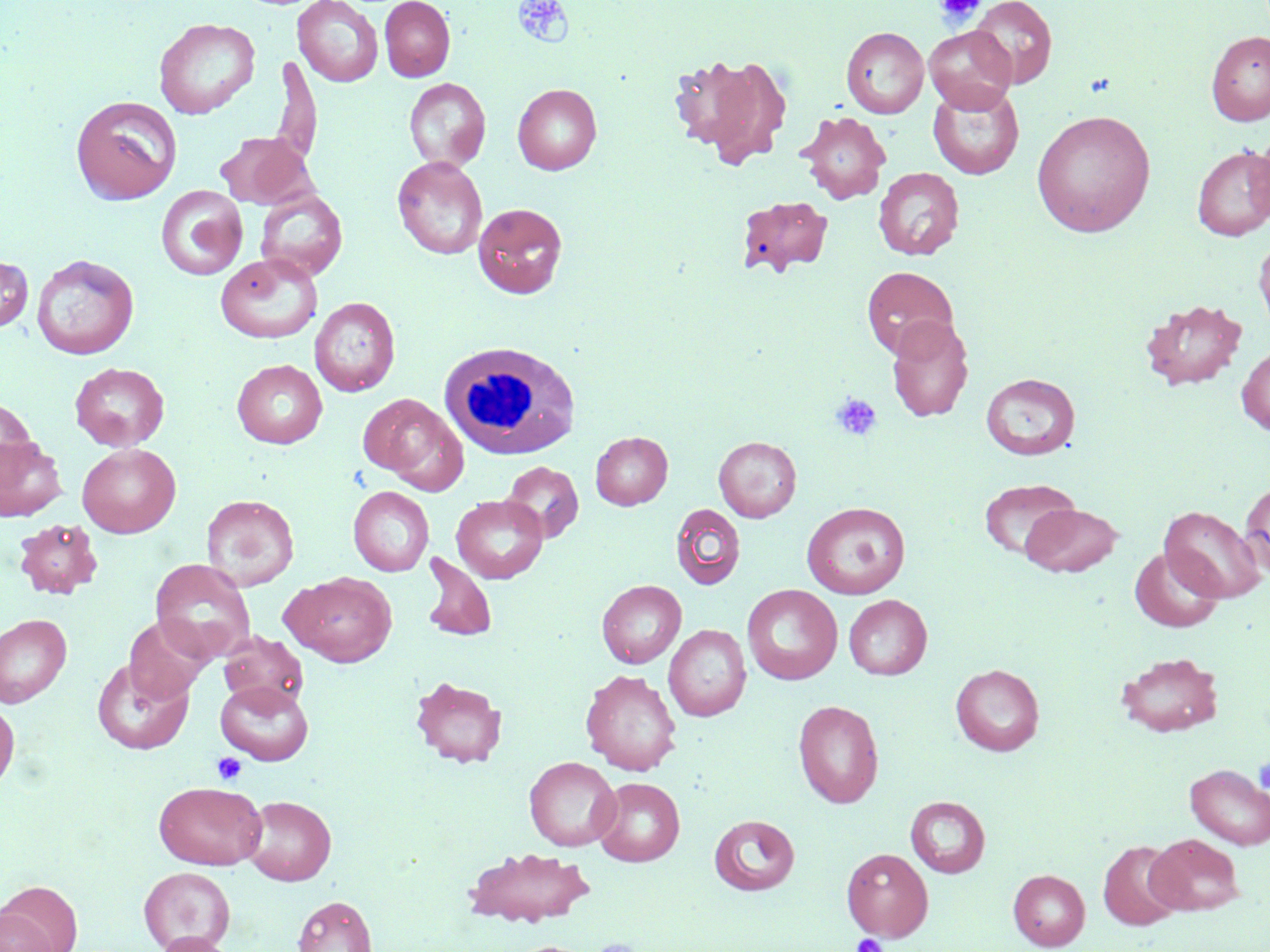

Approximate bounding boxes as named x1/y1/x2/y2 corners in pixels. Uninfected red blood cell locations: (x1=293, y1=0, x2=384, y2=87), (x1=380, y1=0, x2=455, y2=82), (x1=969, y1=0, x2=1057, y2=88), (x1=154, y1=17, x2=260, y2=119), (x1=924, y1=26, x2=1017, y2=113), (x1=841, y1=27, x2=929, y2=119), (x1=1206, y1=31, x2=1270, y2=125), (x1=668, y1=51, x2=793, y2=168), (x1=270, y1=55, x2=322, y2=169), (x1=404, y1=78, x2=491, y2=171), (x1=928, y1=83, x2=1024, y2=180), (x1=513, y1=84, x2=601, y2=175), (x1=71, y1=95, x2=181, y2=204), (x1=1031, y1=109, x2=1156, y2=237), (x1=797, y1=111, x2=891, y2=204), (x1=215, y1=131, x2=314, y2=209), (x1=1249, y1=131, x2=1270, y2=228), (x1=1192, y1=145, x2=1270, y2=241), (x1=392, y1=156, x2=488, y2=259), (x1=874, y1=167, x2=964, y2=260), (x1=156, y1=185, x2=248, y2=281), (x1=256, y1=189, x2=348, y2=282), (x1=738, y1=195, x2=833, y2=277), (x1=473, y1=202, x2=568, y2=299), (x1=1254, y1=235, x2=1270, y2=335), (x1=216, y1=253, x2=322, y2=343), (x1=0, y1=254, x2=33, y2=332), (x1=31, y1=254, x2=139, y2=359), (x1=862, y1=266, x2=958, y2=358), (x1=310, y1=296, x2=400, y2=397), (x1=1141, y1=299, x2=1247, y2=390), (x1=886, y1=316, x2=974, y2=421), (x1=1237, y1=346, x2=1270, y2=435), (x1=232, y1=359, x2=327, y2=448), (x1=70, y1=362, x2=169, y2=451), (x1=981, y1=372, x2=1081, y2=460), (x1=359, y1=393, x2=466, y2=490), (x1=0, y1=399, x2=37, y2=485), (x1=591, y1=431, x2=672, y2=510), (x1=714, y1=436, x2=801, y2=522), (x1=0, y1=437, x2=67, y2=521), (x1=77, y1=443, x2=181, y2=537), (x1=502, y1=461, x2=584, y2=543), (x1=978, y1=478, x2=1080, y2=561), (x1=1240, y1=480, x2=1270, y2=580), (x1=348, y1=486, x2=433, y2=576), (x1=201, y1=494, x2=299, y2=591), (x1=452, y1=495, x2=548, y2=583), (x1=802, y1=502, x2=910, y2=599), (x1=1020, y1=503, x2=1124, y2=576), (x1=671, y1=504, x2=745, y2=590), (x1=1159, y1=506, x2=1265, y2=603), (x1=14, y1=519, x2=102, y2=599), (x1=1130, y1=546, x2=1224, y2=632), (x1=419, y1=553, x2=497, y2=642), (x1=150, y1=559, x2=256, y2=663), (x1=283, y1=571, x2=397, y2=667), (x1=596, y1=579, x2=686, y2=668), (x1=742, y1=584, x2=843, y2=685), (x1=844, y1=595, x2=932, y2=679), (x1=0, y1=614, x2=71, y2=708), (x1=124, y1=615, x2=212, y2=704), (x1=664, y1=624, x2=751, y2=721), (x1=219, y1=631, x2=307, y2=709), (x1=1117, y1=651, x2=1223, y2=737), (x1=92, y1=659, x2=193, y2=754), (x1=950, y1=664, x2=1044, y2=755), (x1=581, y1=669, x2=682, y2=775), (x1=409, y1=676, x2=508, y2=768), (x1=215, y1=679, x2=314, y2=764), (x1=0, y1=699, x2=19, y2=793), (x1=793, y1=699, x2=884, y2=808), (x1=524, y1=756, x2=622, y2=851), (x1=1185, y1=764, x2=1270, y2=849), (x1=592, y1=777, x2=685, y2=866), (x1=153, y1=781, x2=266, y2=869), (x1=242, y1=795, x2=336, y2=885), (x1=905, y1=796, x2=991, y2=878), (x1=709, y1=814, x2=800, y2=895), (x1=1146, y1=834, x2=1244, y2=916), (x1=1097, y1=840, x2=1184, y2=931), (x1=463, y1=846, x2=597, y2=927), (x1=841, y1=848, x2=933, y2=942), (x1=139, y1=866, x2=235, y2=951), (x1=1009, y1=869, x2=1090, y2=950), (x1=0, y1=881, x2=82, y2=952), (x1=293, y1=895, x2=377, y2=952), (x1=0, y1=907, x2=56, y2=952), (x1=152, y1=932, x2=236, y2=952). White blood cell locations: (x1=440, y1=341, x2=580, y2=460). Platelet locations: (x1=935, y1=0, x2=986, y2=25), (x1=511, y1=1, x2=576, y2=48), (x1=831, y1=393, x2=883, y2=442), (x1=213, y1=752, x2=246, y2=785), (x1=1253, y1=758, x2=1270, y2=795), (x1=852, y1=933, x2=886, y2=952), (x1=589, y1=938, x2=647, y2=952). Slide-level diagnosis: no evidence of blood parasites. Image is 1270×952 pixels. May-Grünwald-Giemsa stain. Single field of view. Optical microscopy. Thin blood film. Captured at 1000x magnification.